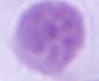
Micrograph. 1000x magnification. An erythrocyte is shown.